Locate every blood parasite and identify its species.
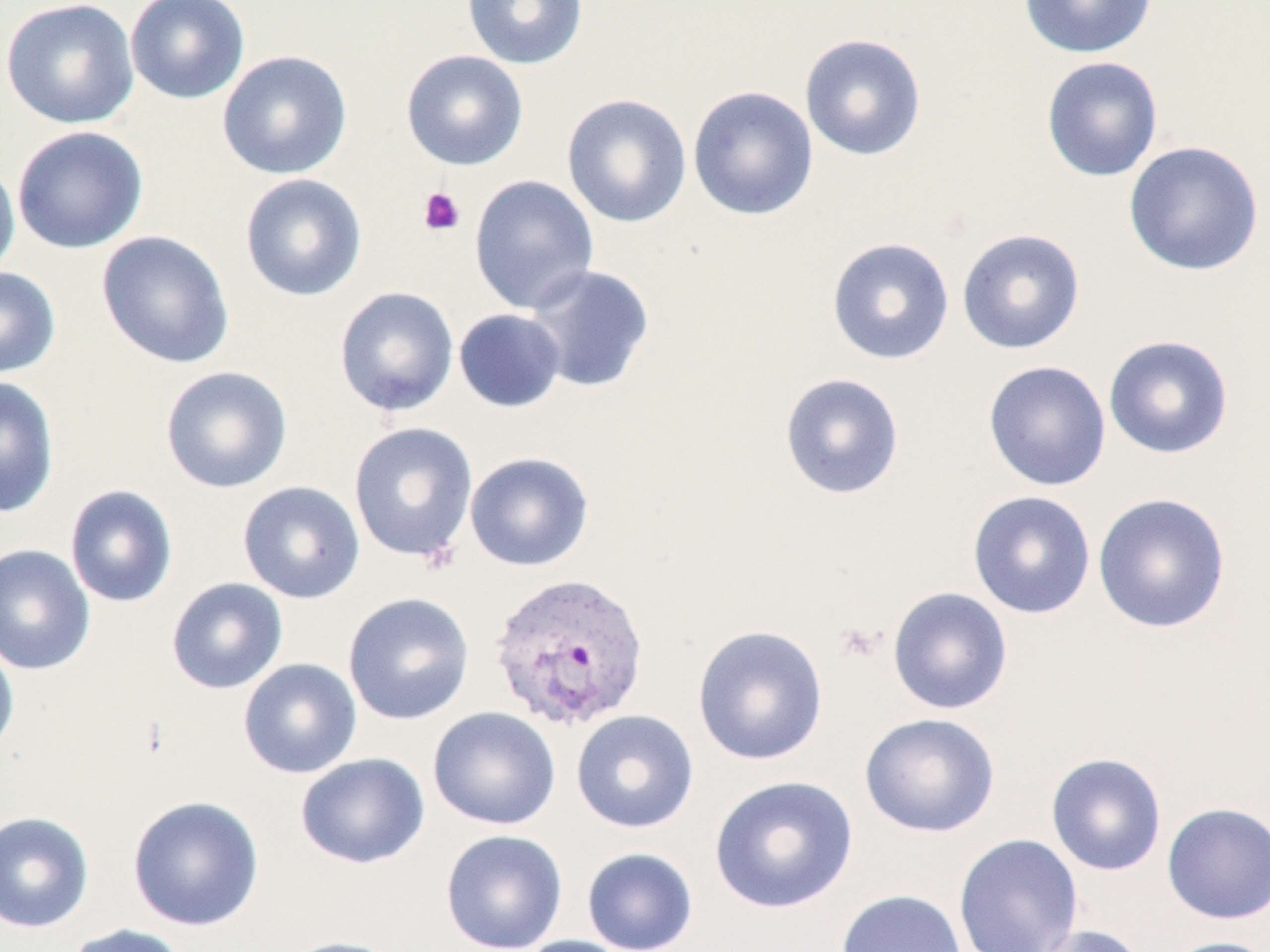
Approximate bounding boxes as [x1, y1, x2, y2] in pixels.
Plasmodium vivax-infected red blood cells: [488, 570, 651, 732].
No Plasmodium falciparum, Plasmodium ovale, Plasmodium malariae, Babesia divergens, or Trypanosoma brucei observed.

slide-level diagnosis = Plasmodium vivax
image size = 1270×952 pixels
platelet locations = approximate bounding boxes as [x1, y1, x2, y2] in pixels: [418, 187, 465, 236], [834, 621, 884, 665]
magnification = 1000x
uninfected red blood cell locations = approximate bounding boxes as [x1, y1, x2, y2] in pixels: [1, 0, 140, 129], [125, 0, 250, 104], [461, 0, 588, 70], [1018, 0, 1157, 60], [799, 32, 927, 161], [217, 50, 353, 180], [400, 50, 529, 171], [1040, 56, 1163, 183], [687, 85, 819, 221], [561, 93, 692, 228], [11, 126, 148, 254], [1122, 140, 1265, 277], [0, 158, 20, 281], [239, 173, 368, 301], [469, 174, 600, 314], [956, 228, 1086, 355], [96, 230, 234, 368], [826, 236, 955, 365], [524, 264, 656, 393], [0, 266, 61, 380], [333, 286, 459, 417], [453, 308, 567, 413], [1102, 334, 1235, 460], [982, 360, 1112, 491], [160, 366, 292, 493], [779, 372, 905, 501], [0, 376, 60, 519], [348, 421, 479, 564], [464, 451, 595, 572], [237, 481, 366, 603], [64, 484, 179, 608], [966, 490, 1097, 619], [1092, 492, 1231, 634], [0, 544, 96, 675], [165, 577, 288, 695], [886, 586, 1014, 715], [343, 592, 475, 725], [691, 623, 829, 766], [0, 638, 20, 761], [238, 658, 362, 779], [428, 706, 561, 831], [570, 709, 699, 833], [859, 712, 1000, 838], [295, 752, 430, 869], [1045, 752, 1167, 876], [709, 774, 858, 914], [126, 795, 265, 931], [1161, 802, 1270, 924], [0, 811, 95, 933], [439, 829, 568, 952], [953, 833, 1083, 952], [581, 847, 698, 952], [835, 888, 967, 952], [61, 923, 190, 952], [1029, 924, 1150, 952], [513, 935, 640, 952], [279, 936, 405, 952], [1159, 936, 1270, 952]
preparation = thin blood smear
stain = May-Grünwald-Giemsa
field of view = one of a larger specimen
modality = light microscopy